Evaluate for Plasmodium parasites.
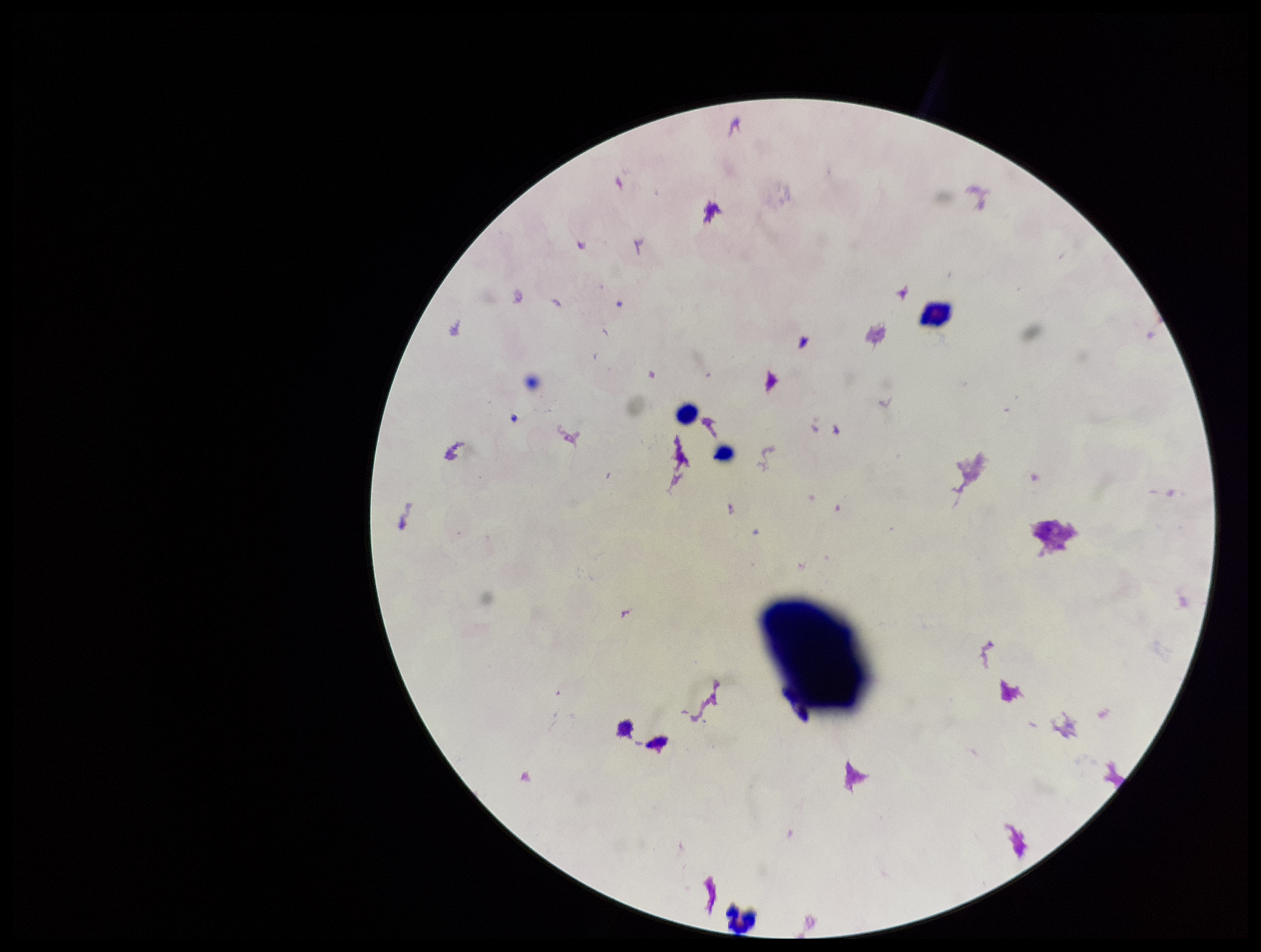

None detected.

Smartphone photograph taken through the eyepiece of a microscope. Parasite count: 0. Image is 1261×952 pixels. Leukocyte count: 4. Stained with Giemsa. Preparation: thick smear. Patient malaria status: negative. Single field of view.